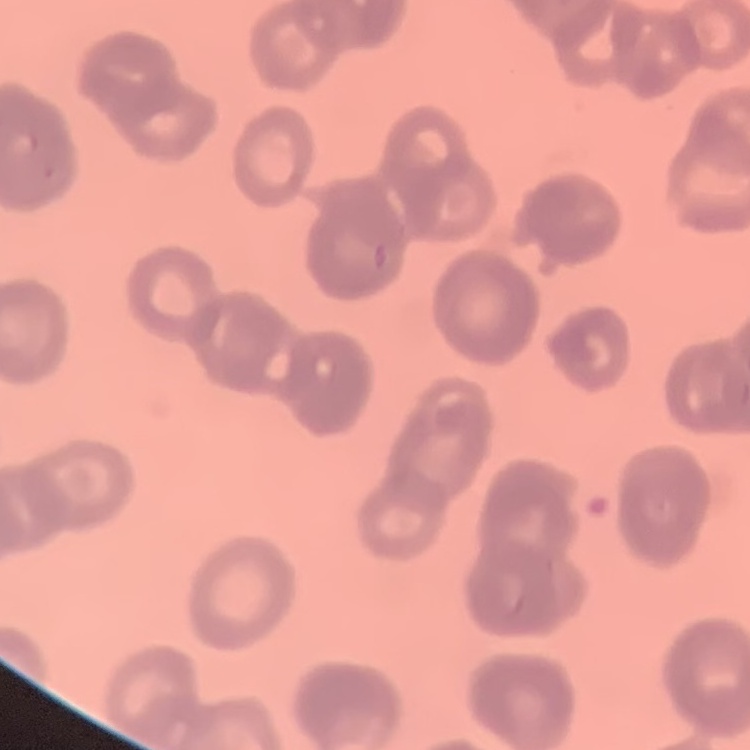 The red blood cells exhibit rouleaux formation. Field's or Giemsa stain. Square crop of a larger photomicrograph. Thin peripheral smear.